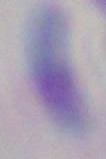
magnification = 1000x
identification = Toxoplasma gondii
modality = micrograph